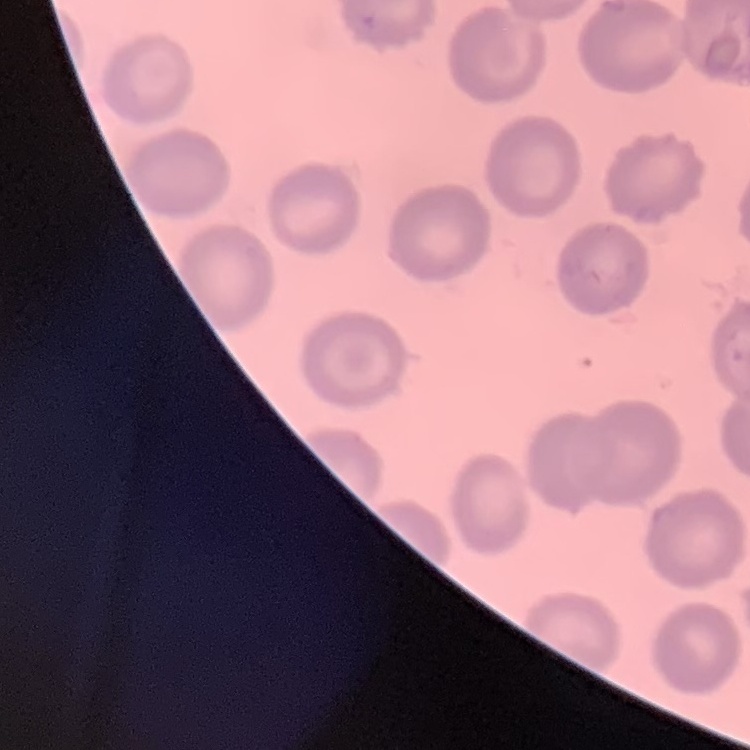 The red blood cells show no rouleaux formation. Field's or Giemsa stain. One tile cut from a larger photomicrograph. Thin blood smear.